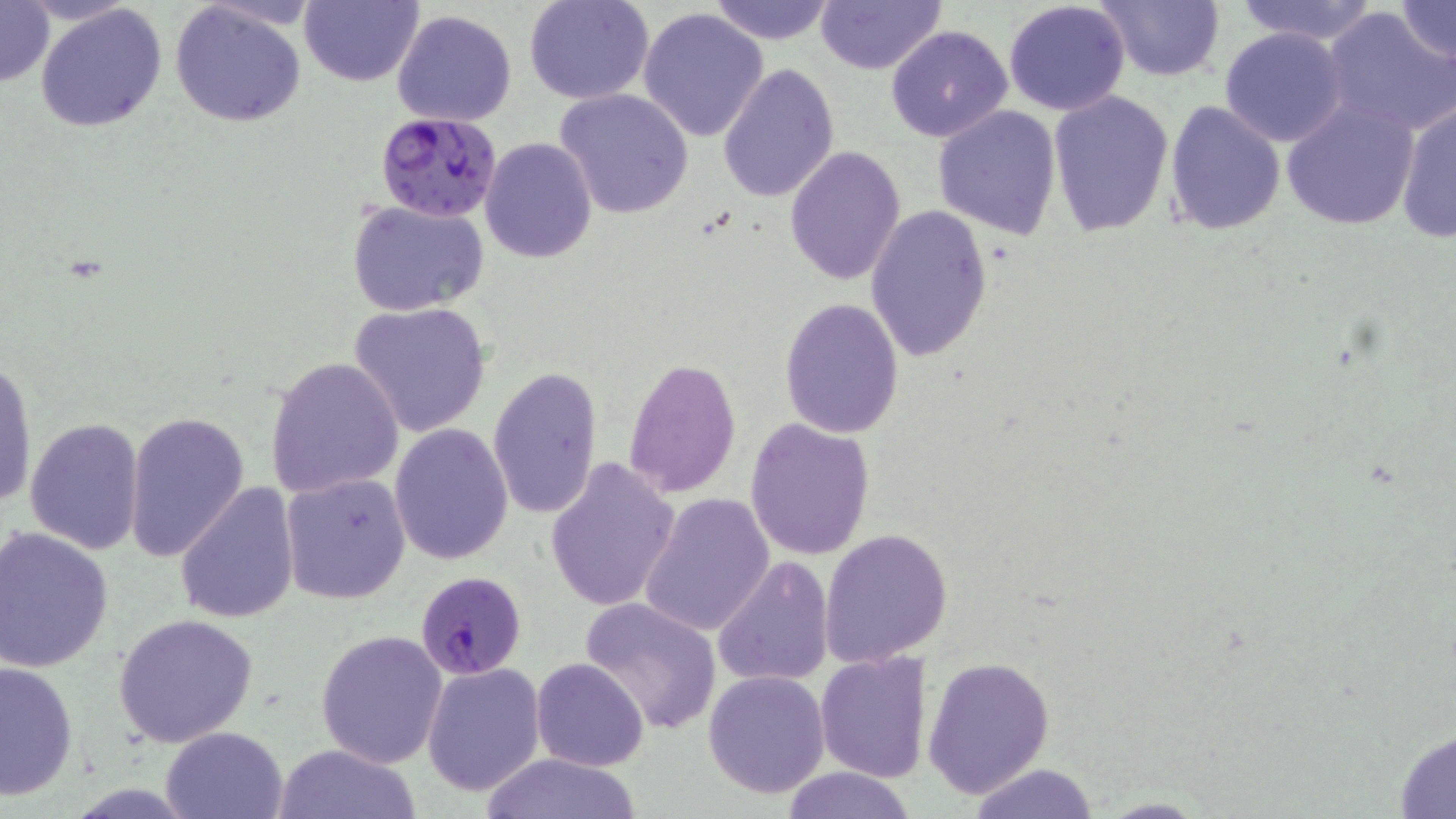

slide-level diagnosis = Plasmodium falciparum
field of view = single
Plasmodium falciparum-infected red blood cell locations = approximate bounding boxes as named x1/y1/x2/y2 corners in pixels: (x1=376, y1=112, x2=501, y2=221), (x1=415, y1=571, x2=526, y2=679)
preparation = thin blood smear
uninfected red blood cell locations = approximate bounding boxes as named x1/y1/x2/y2 corners in pixels: (x1=0, y1=0, x2=53, y2=88), (x1=300, y1=0, x2=421, y2=87), (x1=524, y1=0, x2=655, y2=104), (x1=706, y1=0, x2=840, y2=45), (x1=816, y1=0, x2=946, y2=75), (x1=1003, y1=0, x2=1132, y2=115), (x1=1093, y1=0, x2=1224, y2=82), (x1=1233, y1=0, x2=1382, y2=46), (x1=1392, y1=0, x2=1456, y2=67), (x1=168, y1=4, x2=307, y2=126), (x1=35, y1=5, x2=169, y2=133), (x1=1322, y1=5, x2=1456, y2=135), (x1=637, y1=7, x2=769, y2=143), (x1=392, y1=9, x2=518, y2=127), (x1=885, y1=24, x2=1014, y2=143), (x1=1219, y1=27, x2=1349, y2=148), (x1=718, y1=63, x2=840, y2=202), (x1=555, y1=88, x2=695, y2=219), (x1=1048, y1=91, x2=1176, y2=236), (x1=1280, y1=98, x2=1422, y2=230), (x1=1394, y1=100, x2=1455, y2=243), (x1=1164, y1=101, x2=1286, y2=234), (x1=932, y1=104, x2=1062, y2=239), (x1=480, y1=138, x2=596, y2=262), (x1=784, y1=145, x2=906, y2=286), (x1=347, y1=198, x2=490, y2=317), (x1=865, y1=206, x2=993, y2=364), (x1=779, y1=297, x2=905, y2=437), (x1=349, y1=301, x2=492, y2=437), (x1=263, y1=356, x2=405, y2=498), (x1=1, y1=357, x2=36, y2=510), (x1=622, y1=357, x2=742, y2=497), (x1=487, y1=366, x2=601, y2=518), (x1=124, y1=411, x2=250, y2=566), (x1=24, y1=417, x2=146, y2=556), (x1=744, y1=418, x2=876, y2=560), (x1=389, y1=422, x2=514, y2=564), (x1=543, y1=456, x2=682, y2=613), (x1=281, y1=472, x2=410, y2=604), (x1=174, y1=482, x2=302, y2=625), (x1=640, y1=492, x2=775, y2=637), (x1=2, y1=527, x2=116, y2=672), (x1=819, y1=528, x2=953, y2=668), (x1=712, y1=555, x2=835, y2=688), (x1=577, y1=596, x2=725, y2=737), (x1=112, y1=613, x2=260, y2=747), (x1=315, y1=629, x2=448, y2=767), (x1=814, y1=650, x2=931, y2=783), (x1=532, y1=657, x2=648, y2=771), (x1=923, y1=657, x2=1054, y2=799), (x1=0, y1=658, x2=78, y2=802), (x1=421, y1=661, x2=546, y2=796), (x1=701, y1=668, x2=831, y2=799), (x1=161, y1=725, x2=290, y2=818), (x1=1393, y1=728, x2=1456, y2=818), (x1=275, y1=744, x2=422, y2=819), (x1=480, y1=751, x2=643, y2=819), (x1=966, y1=762, x2=1101, y2=818), (x1=777, y1=765, x2=918, y2=819)
modality = light microscopy
magnification = 1000x
image size = 1456×819 pixels
stain = May-Grünwald-Giemsa